Locate every uninfected red blood cell.
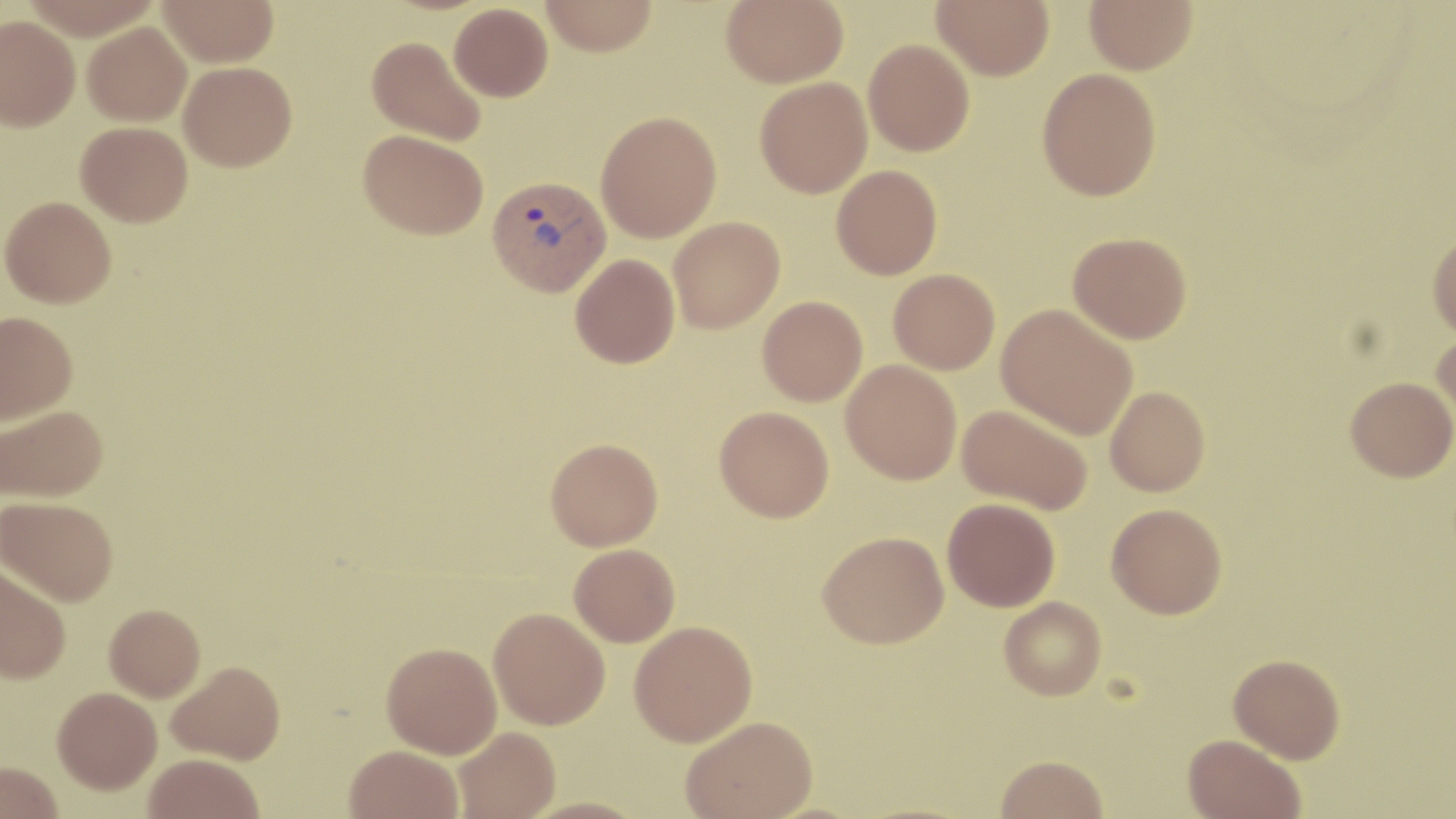
Approximate bounding boxes as (x1, y1, x2, y2) in pixels.
Uninfected red blood cells: (158, 0, 279, 67), (540, 0, 658, 56), (721, 0, 848, 87), (932, 0, 1054, 80), (1083, 0, 1198, 74), (449, 3, 553, 101), (0, 15, 80, 131), (82, 22, 191, 126), (367, 35, 487, 146), (863, 39, 974, 156), (178, 61, 297, 171), (1037, 67, 1161, 201), (755, 77, 872, 198), (596, 111, 722, 242), (76, 121, 193, 226), (359, 129, 488, 239), (831, 164, 942, 279), (1, 196, 117, 307), (668, 216, 785, 333), (1068, 232, 1191, 343), (1427, 232, 1456, 340), (570, 253, 679, 368), (888, 268, 1000, 374), (758, 296, 867, 406), (997, 304, 1137, 440), (0, 311, 78, 425), (1431, 330, 1456, 436), (841, 360, 962, 484), (1345, 376, 1456, 481), (1105, 386, 1210, 496), (957, 403, 1093, 515), (1, 405, 108, 503), (715, 406, 834, 522), (545, 438, 663, 551), (1, 495, 118, 606), (942, 498, 1060, 611), (1106, 503, 1227, 618), (818, 530, 949, 648), (568, 544, 679, 646), (0, 561, 71, 683), (999, 596, 1107, 700), (104, 604, 205, 701), (488, 607, 611, 729), (629, 620, 757, 746), (381, 642, 502, 758), (1228, 653, 1345, 763), (167, 660, 285, 764), (52, 686, 162, 793), (680, 715, 818, 819), (454, 726, 561, 818), (1183, 734, 1306, 819), (345, 745, 463, 819), (143, 753, 265, 818), (995, 754, 1108, 818), (0, 761, 63, 819).

Plasmodium vivax-infected red blood cell locations: (487, 175, 611, 296). Slide-level diagnosis: Plasmodium vivax. Thin blood smear. Image is 1456×819 pixels. May-Grünwald-Giemsa stain. 1000x magnification. Optical microscopy. One field of a larger specimen.